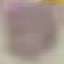
Malaria status: uninfected. Giemsa stain. Photographed with a smartphone camera at the microscope eyepiece. Cell patch, automatically extracted from a larger field of view and resized to 64 × 64 pixels. Thin blood smear.